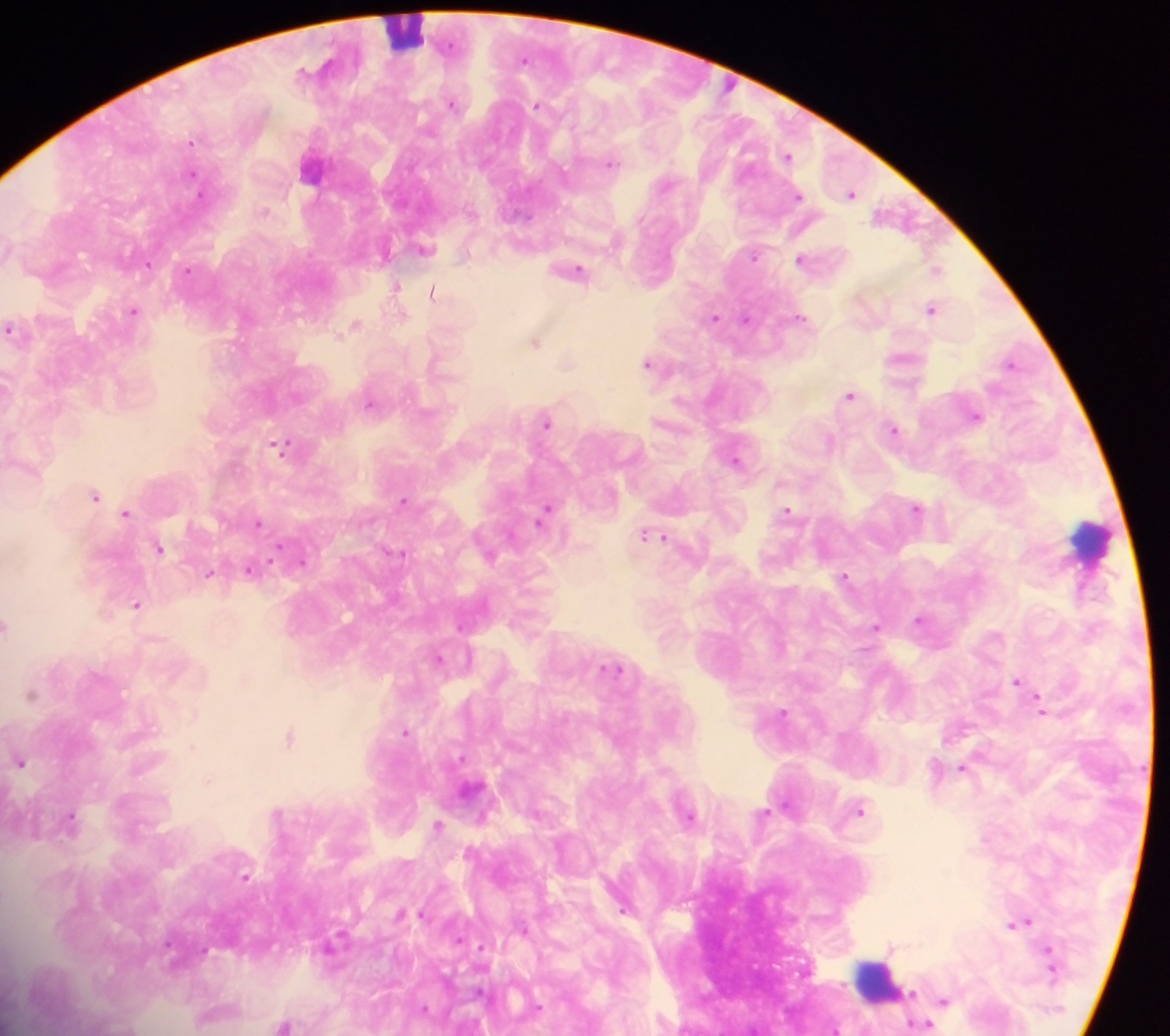
Approximate centers as (x, y) in pixels.
Summary:
  - Malaria parasite locations: (525, 57), (453, 103), (537, 105), (192, 141), (788, 155), (612, 162), (194, 173), (851, 192), (798, 195), (265, 210), (425, 248), (754, 255), (800, 258), (148, 263), (578, 269), (187, 270), (937, 270), (396, 286), (432, 292), (932, 308), (133, 309), (403, 315), (800, 316), (715, 317), (746, 318), (355, 323), (10, 328), (536, 341), (1010, 361), (569, 362), (648, 363), (849, 394), (371, 402), (976, 415), (547, 421), (894, 428), (829, 441), (280, 445), (736, 459), (95, 495), (404, 500), (917, 507), (787, 509), (126, 512), (544, 512), (258, 522), (651, 534), (664, 536), (159, 547), (400, 553), (302, 561), (251, 569), (210, 573), (845, 575), (137, 604), (920, 619), (7, 625), (461, 626), (877, 626), (439, 658), (616, 669), (1017, 680), (31, 694), (1042, 708), (783, 711), (405, 731), (290, 737), (461, 756), (21, 761), (962, 767), (860, 809), (765, 813), (690, 815), (483, 816), (72, 817), (437, 825), (246, 876), (624, 909), (402, 913), (1023, 921), (482, 946), (890, 946), (909, 992), (944, 1000), (283, 1024), (923, 1024)
  - Leukocyte locations: (408, 34), (1090, 541), (880, 978)
  - Preparation: thick blood film
  - Country: Ghana
  - Capture: mobile-phone photograph through a microscope
  - Image size: 1170×1036 pixels
  - Field of view: single